Name the blood parasite species.
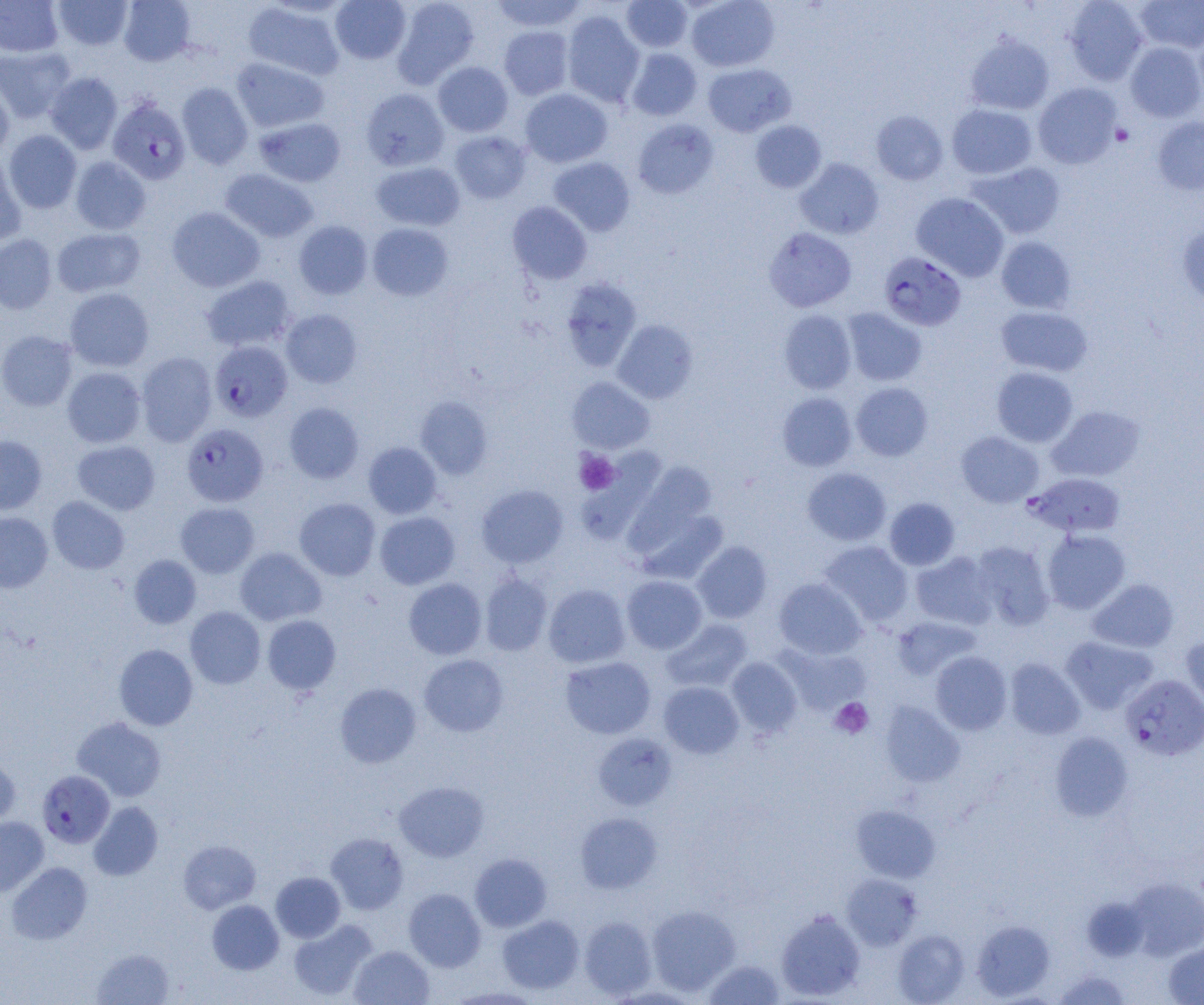
Plasmodium falciparum.

preparation = thin blood film
magnification = 1000x
image size = 1204×1005 pixels
modality = optical microscopy
uninfected red blood cell locations = approximate bounding boxes as (x1,y1)-(x2,y2) corner pairs in pixels: (0,0)-(64,57), (53,0)-(133,50), (119,0)-(196,66), (330,0)-(411,64), (392,0)-(480,87), (491,0)-(587,32), (686,0)-(780,72), (1064,0)-(1148,85), (1134,0)-(1204,53), (621,1)-(692,52), (243,2)-(345,80), (561,10)-(645,107), (499,25)-(574,99), (1193,28)-(1204,111), (965,33)-(1055,116), (1125,42)-(1204,122), (0,46)-(76,124), (626,48)-(702,121), (231,57)-(329,133), (433,61)-(513,136), (703,63)-(796,136), (45,72)-(123,154), (0,81)-(14,161), (177,82)-(253,169), (1033,82)-(1122,169), (361,88)-(449,171), (520,88)-(612,168), (947,104)-(1037,180), (871,110)-(948,185), (254,117)-(346,187), (1152,117)-(1204,195), (632,119)-(718,199), (750,120)-(826,193), (4,130)-(82,213), (449,131)-(531,203), (0,156)-(26,247), (70,157)-(151,234), (548,157)-(635,236), (794,158)-(884,239), (371,161)-(465,231), (967,161)-(1066,239), (220,168)-(318,243), (911,193)-(1009,281), (507,201)-(592,284), (167,207)-(264,292), (294,220)-(373,299), (367,223)-(453,301), (1177,223)-(1204,309), (52,227)-(146,298), (763,227)-(857,312), (0,234)-(57,314), (996,237)-(1076,313), (200,275)-(296,352), (560,277)-(642,372), (64,287)-(154,372), (996,306)-(1093,377), (842,308)-(927,386), (281,309)-(362,388), (778,310)-(856,394), (611,319)-(698,404), (0,330)-(78,411), (136,352)-(217,446), (62,367)-(146,448), (992,367)-(1078,447), (566,376)-(655,454), (851,382)-(933,461), (777,392)-(857,471), (415,396)-(493,480), (284,402)-(364,483), (1046,405)-(1145,482), (957,431)-(1043,507), (0,435)-(47,514), (72,440)-(160,515), (363,442)-(442,518), (576,450)-(666,543), (624,463)-(721,570), (802,467)-(891,546), (476,484)-(569,568), (47,496)-(129,574), (294,497)-(380,580), (884,497)-(960,570), (175,502)-(260,578), (375,511)-(460,590), (0,512)-(53,593), (1042,529)-(1131,614), (692,541)-(772,623), (819,541)-(914,627), (970,541)-(1054,629), (235,547)-(326,625), (910,551)-(997,629), (129,555)-(201,628), (480,572)-(552,656), (622,575)-(708,653), (774,577)-(866,660), (403,578)-(487,659), (1088,579)-(1178,653), (543,584)-(631,668), (185,606)-(265,689), (261,615)-(341,694), (892,616)-(981,679), (661,618)-(752,692), (1181,634)-(1204,716), (1061,636)-(1158,714), (114,644)-(198,730), (776,644)-(871,716), (930,651)-(1012,735), (419,654)-(508,737), (560,656)-(656,739), (726,657)-(803,738), (1005,658)-(1085,739), (658,681)-(744,759), (335,682)-(422,767), (880,701)-(965,787), (72,716)-(167,802), (1049,731)-(1134,821), (593,733)-(677,810), (0,755)-(20,827), (394,780)-(489,862), (88,801)-(163,880), (851,804)-(940,882), (575,812)-(661,894), (0,816)-(49,896), (326,832)-(408,914), (178,840)-(261,914), (469,853)-(552,932), (6,861)-(93,944), (271,872)-(345,942), (841,873)-(923,949), (1129,877)-(1204,961), (404,888)-(486,971), (1082,896)-(1149,961), (207,900)-(284,974), (646,904)-(741,996), (776,908)-(866,1001), (498,915)-(584,994), (579,916)-(657,999), (288,919)-(377,1000), (972,919)-(1054,1000), (893,930)-(969,1005), (1164,941)-(1204,1004), (349,945)-(434,1005), (91,948)-(174,1005), (702,959)-(785,1004), (1054,971)-(1131,1005), (445,986)-(544,1004)
platelet locations = approximate bounding boxes as (x1,y1)-(x2,y2) corner pairs in pixels: (1111,124)-(1134,147), (574,449)-(620,495), (830,698)-(873,739)
Plasmodium falciparum-infected red blood cell locations = approximate bounding boxes as (x1,y1)-(x2,y2) corner pairs in pixels: (108,97)-(190,184), (879,251)-(966,331), (210,340)-(293,422), (181,423)-(268,507), (1028,472)-(1125,538), (1121,674)-(1204,761), (37,770)-(115,848)
field of view = one of a larger specimen